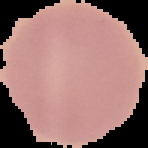
image type = segmented cell region on a black background
preparation = thin blood film
result = negative for malaria parasites
image size = 148×148 pixels